Point out leukocytes.
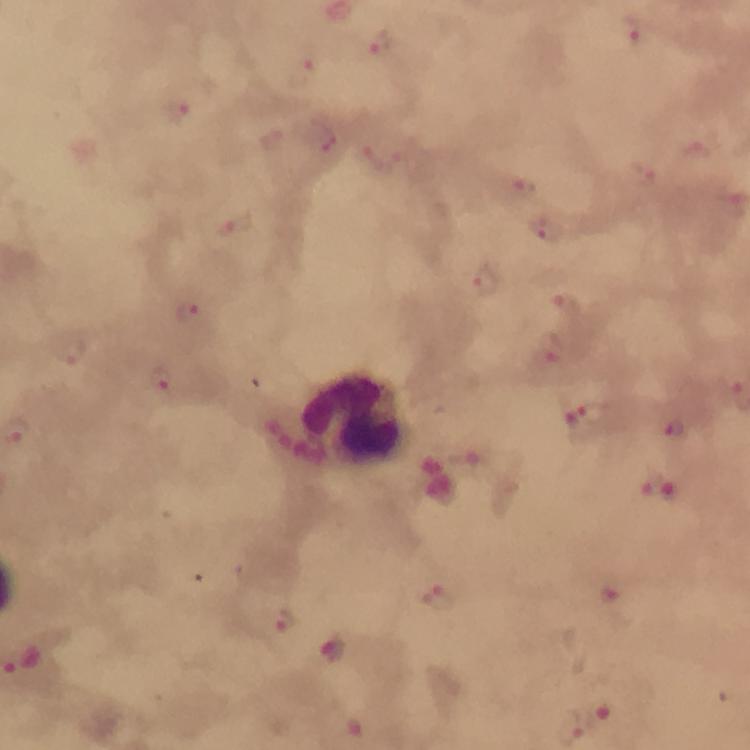
Approximate centers as {x, y} in pixels.
Leukocytes: {352, 417}.

malaria parasite locations = approximate centers as {x, y} in pixels: {633, 35}, {379, 43}, {306, 70}, {181, 112}, {699, 151}, {384, 157}, {645, 170}, {524, 188}, {235, 227}, {545, 227}, {485, 284}, {565, 304}, {190, 314}, {550, 350}, {70, 352}, {162, 380}, {583, 417}, {673, 430}, {470, 457}, {659, 487}, {608, 596}, {436, 598}, {283, 622}, {333, 650}
image size = 750×750 pixels
preparation = thick blood film
capture = smartphone photograph through a microscope
immersion oil = applied
cropped from = a single field of view
context = from a diagnostic examination for malaria
magnification = 100x
stain = Giemsa